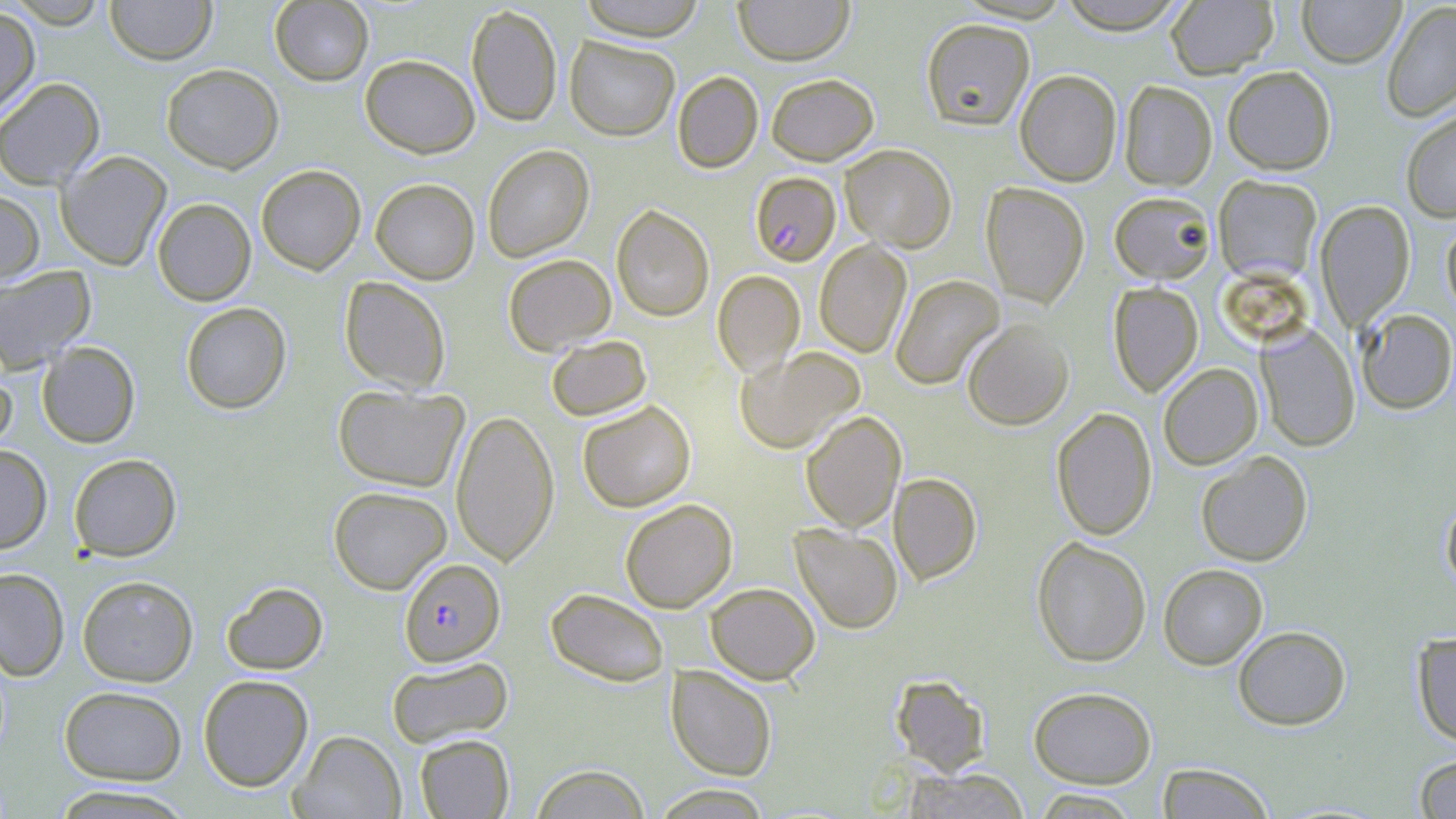

Summary:
  - Coordinate format: approximate bounding boxes as named x1/y1/x2/y2 corners in pixels
  - Uninfected red blood cell locations: (x1=105, y1=0, x2=216, y2=65), (x1=269, y1=0, x2=374, y2=86), (x1=578, y1=0, x2=706, y2=40), (x1=734, y1=0, x2=855, y2=65), (x1=1056, y1=0, x2=1188, y2=34), (x1=1166, y1=0, x2=1278, y2=78), (x1=1297, y1=0, x2=1406, y2=67), (x1=6, y1=1, x2=109, y2=28), (x1=1382, y1=2, x2=1456, y2=121), (x1=466, y1=5, x2=562, y2=127), (x1=0, y1=6, x2=40, y2=122), (x1=920, y1=18, x2=1035, y2=130), (x1=564, y1=35, x2=680, y2=141), (x1=360, y1=54, x2=480, y2=158), (x1=161, y1=63, x2=284, y2=173), (x1=1222, y1=65, x2=1336, y2=175), (x1=1015, y1=69, x2=1121, y2=186), (x1=672, y1=71, x2=763, y2=173), (x1=766, y1=73, x2=879, y2=165), (x1=0, y1=77, x2=105, y2=189), (x1=1119, y1=80, x2=1217, y2=191), (x1=1401, y1=110, x2=1456, y2=222), (x1=839, y1=143, x2=956, y2=252), (x1=482, y1=144, x2=594, y2=262), (x1=56, y1=151, x2=172, y2=271), (x1=256, y1=165, x2=365, y2=275), (x1=1213, y1=175, x2=1322, y2=283), (x1=370, y1=178, x2=480, y2=285), (x1=981, y1=182, x2=1090, y2=308), (x1=0, y1=190, x2=45, y2=286), (x1=1109, y1=191, x2=1216, y2=283), (x1=152, y1=198, x2=256, y2=306), (x1=1315, y1=200, x2=1415, y2=331), (x1=611, y1=205, x2=714, y2=322), (x1=1442, y1=219, x2=1456, y2=320), (x1=814, y1=240, x2=911, y2=358), (x1=503, y1=253, x2=616, y2=355), (x1=0, y1=266, x2=96, y2=374), (x1=712, y1=270, x2=805, y2=376), (x1=890, y1=274, x2=1004, y2=389), (x1=339, y1=276, x2=451, y2=394), (x1=1108, y1=282, x2=1203, y2=396), (x1=181, y1=302, x2=291, y2=414), (x1=1356, y1=309, x2=1456, y2=414), (x1=962, y1=319, x2=1074, y2=430), (x1=1256, y1=324, x2=1360, y2=452), (x1=545, y1=335, x2=652, y2=422), (x1=37, y1=342, x2=140, y2=448), (x1=734, y1=346, x2=865, y2=454), (x1=0, y1=362, x2=16, y2=456), (x1=1158, y1=363, x2=1263, y2=469), (x1=333, y1=384, x2=468, y2=492), (x1=577, y1=400, x2=696, y2=512), (x1=1051, y1=407, x2=1157, y2=540), (x1=451, y1=409, x2=559, y2=566), (x1=800, y1=411, x2=906, y2=532), (x1=0, y1=445, x2=52, y2=553), (x1=1195, y1=451, x2=1313, y2=566), (x1=68, y1=453, x2=181, y2=561), (x1=889, y1=472, x2=982, y2=585), (x1=328, y1=486, x2=452, y2=594), (x1=1441, y1=496, x2=1456, y2=594), (x1=620, y1=498, x2=738, y2=613), (x1=790, y1=524, x2=903, y2=634), (x1=1032, y1=537, x2=1151, y2=667), (x1=1158, y1=563, x2=1268, y2=669), (x1=0, y1=568, x2=70, y2=681), (x1=77, y1=575, x2=199, y2=687), (x1=221, y1=582, x2=328, y2=675), (x1=705, y1=582, x2=820, y2=685), (x1=545, y1=588, x2=670, y2=687), (x1=1233, y1=625, x2=1351, y2=730), (x1=1412, y1=632, x2=1456, y2=746), (x1=386, y1=656, x2=514, y2=747), (x1=666, y1=665, x2=778, y2=781), (x1=198, y1=674, x2=313, y2=791), (x1=890, y1=674, x2=991, y2=776), (x1=59, y1=685, x2=187, y2=785), (x1=1028, y1=687, x2=1156, y2=787), (x1=290, y1=730, x2=406, y2=818), (x1=415, y1=734, x2=514, y2=818), (x1=1414, y1=753, x2=1456, y2=818), (x1=529, y1=763, x2=651, y2=819), (x1=1155, y1=763, x2=1275, y2=819), (x1=903, y1=767, x2=1030, y2=819), (x1=651, y1=784, x2=773, y2=818), (x1=49, y1=785, x2=196, y2=818), (x1=1032, y1=789, x2=1142, y2=818)
  - Plasmodium falciparum-infected red blood cell locations: (x1=750, y1=172, x2=841, y2=266), (x1=399, y1=558, x2=506, y2=666)
  - Slide-level diagnosis: Plasmodium falciparum
  - Magnification: 1000x
  - Field of view: one of a larger specimen
  - Modality: optical microscopy
  - Image size: 1456×819 pixels
  - Stain: May-Grünwald-Giemsa
  - Preparation: thin blood film